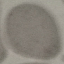

Result: no malaria parasites detected. Acquired by smartphone through the microscope eyepiece. Thin blood film. Automatically extracted cell patch, resized to 64 × 64 pixels. Giemsa stain.